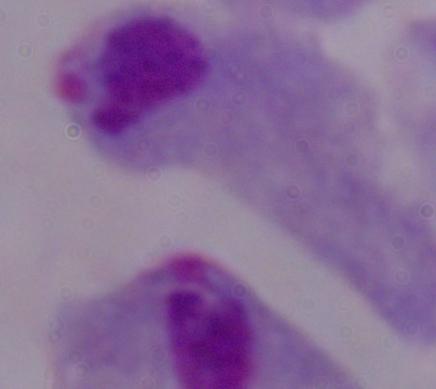 A trichomonad is seen. Photomicrograph. Captured at 1000x magnification.